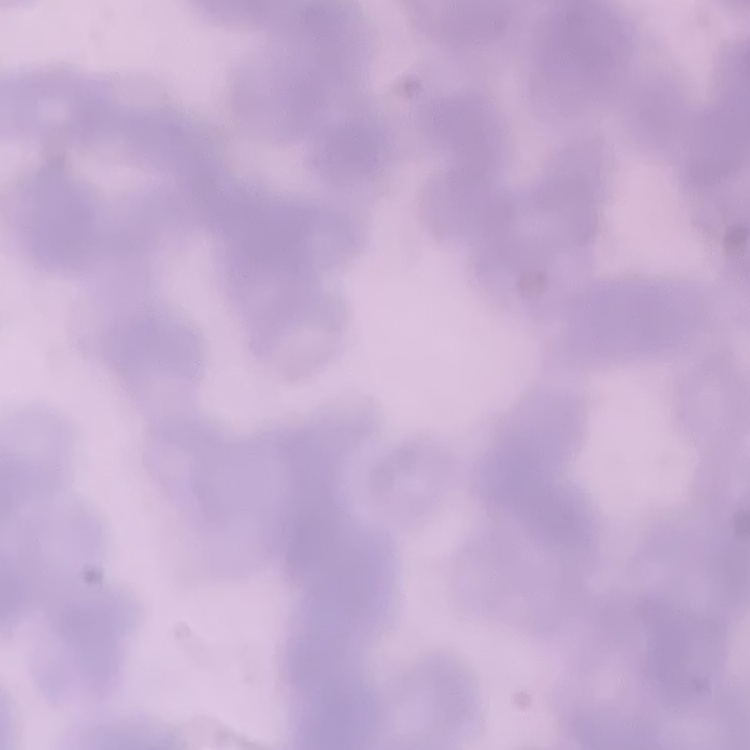
erythrocyte_morphology: rouleaux formation
image_type: square crop of a larger photomicrograph
preparation: thin blood film
stain: Field's or Giemsa